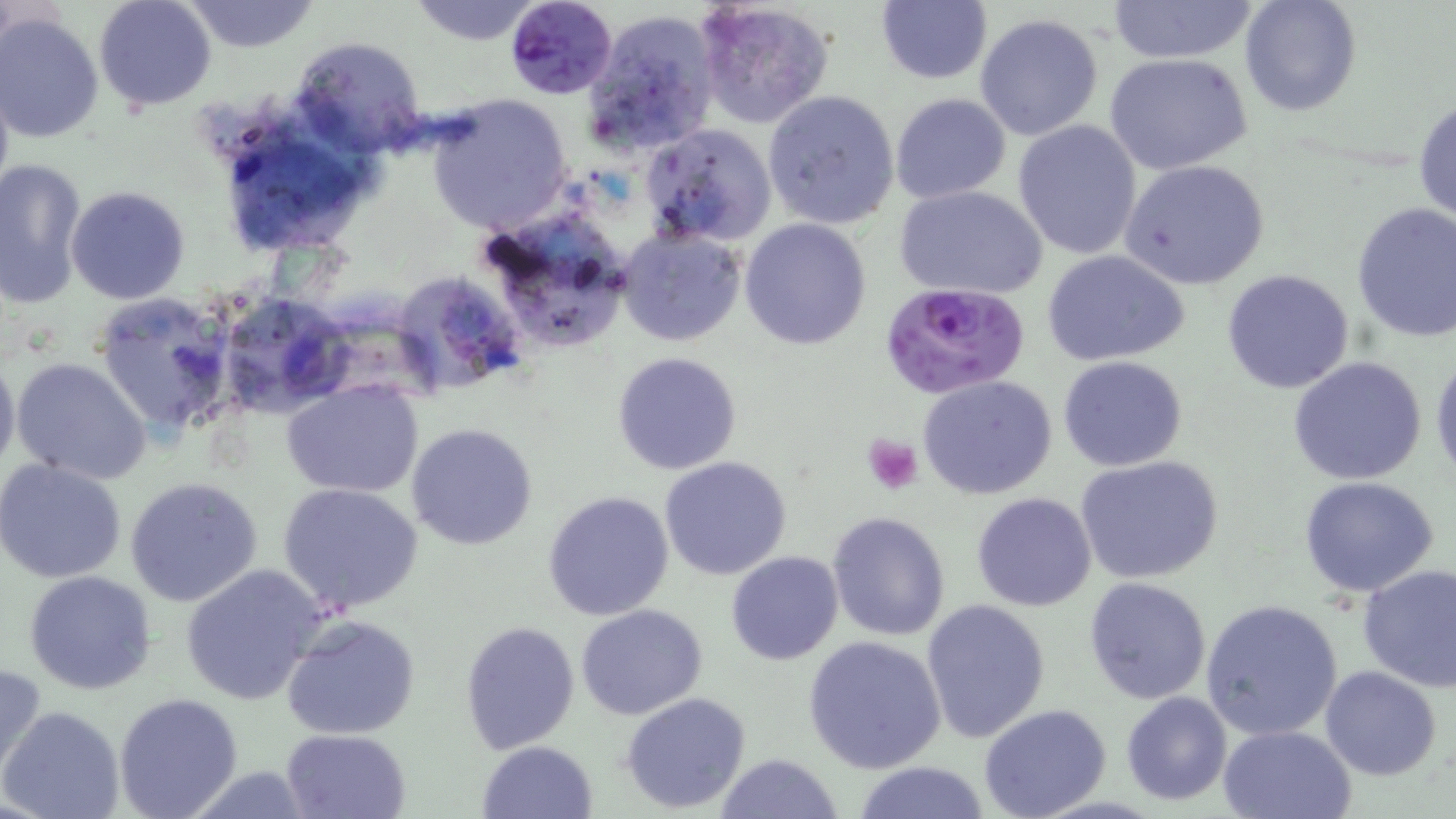
slide_level_diagnosis: Plasmodium falciparum
preparation: thin blood film
field_of_view: single
magnification: 1000x
stain: May-Grünwald-Giemsa
platelet_locations: 'approximate bounding boxes as [x1, y1, x2, y2] in pixels: [861, 433, 924, 495]'
uninfected_red_blood_cell_locations: 'approximate bounding boxes as [x1, y1, x2, y2] in pixels: [93, 0, 218, 112], [181, 0, 321, 53], [406, 0, 545, 45], [692, 0, 836, 130], [875, 0, 992, 85], [1107, 0, 1257, 64], [1238, 0, 1363, 118], [4, 10, 212, 134], [582, 11, 720, 159], [974, 12, 1104, 140], [1, 13, 105, 144], [289, 34, 426, 156], [1103, 52, 1254, 175], [0, 65, 14, 211], [761, 91, 901, 230], [890, 92, 1012, 206], [426, 94, 571, 232], [1413, 95, 1456, 229], [211, 111, 378, 258], [1013, 120, 1142, 260], [639, 123, 778, 247], [0, 157, 88, 308], [1120, 159, 1271, 291], [894, 184, 1048, 301], [66, 185, 191, 305], [1351, 201, 1456, 343], [470, 205, 639, 353], [740, 218, 872, 353], [616, 229, 746, 347], [1044, 251, 1190, 366], [1223, 269, 1354, 393], [389, 270, 530, 399], [214, 287, 357, 421], [93, 291, 240, 435], [0, 348, 21, 479], [612, 351, 742, 475], [1430, 352, 1456, 487], [1059, 356, 1188, 472], [1287, 356, 1427, 485], [11, 357, 153, 485], [921, 366, 1190, 485], [917, 373, 1057, 499], [282, 380, 425, 498], [407, 423, 539, 552], [658, 455, 793, 580], [1074, 455, 1224, 584], [0, 458, 128, 584], [1298, 475, 1441, 599], [125, 477, 264, 607], [277, 482, 425, 614], [542, 490, 675, 621], [971, 492, 1098, 611], [826, 512, 952, 643], [725, 551, 844, 665], [1357, 562, 1456, 693], [179, 563, 330, 707], [23, 569, 157, 694], [1085, 576, 1213, 704], [920, 598, 1051, 745], [1201, 598, 1344, 743], [576, 603, 706, 719], [282, 614, 421, 739], [459, 621, 580, 754], [804, 635, 946, 773], [0, 660, 48, 786], [1320, 666, 1443, 780], [620, 691, 752, 811], [1120, 691, 1232, 805], [112, 692, 243, 819], [978, 703, 1112, 819], [2, 704, 126, 819], [1217, 725, 1357, 818], [281, 729, 410, 818], [477, 739, 598, 818], [715, 753, 843, 819], [850, 761, 993, 818], [180, 765, 317, 818]'
plasmodium_falciparum_infected_red_blood_cell_locations: 'approximate bounding boxes as [x1, y1, x2, y2] in pixels: [504, 0, 617, 100], [880, 283, 1030, 399]'
image_size: 1456×819 pixels
modality: light microscopy